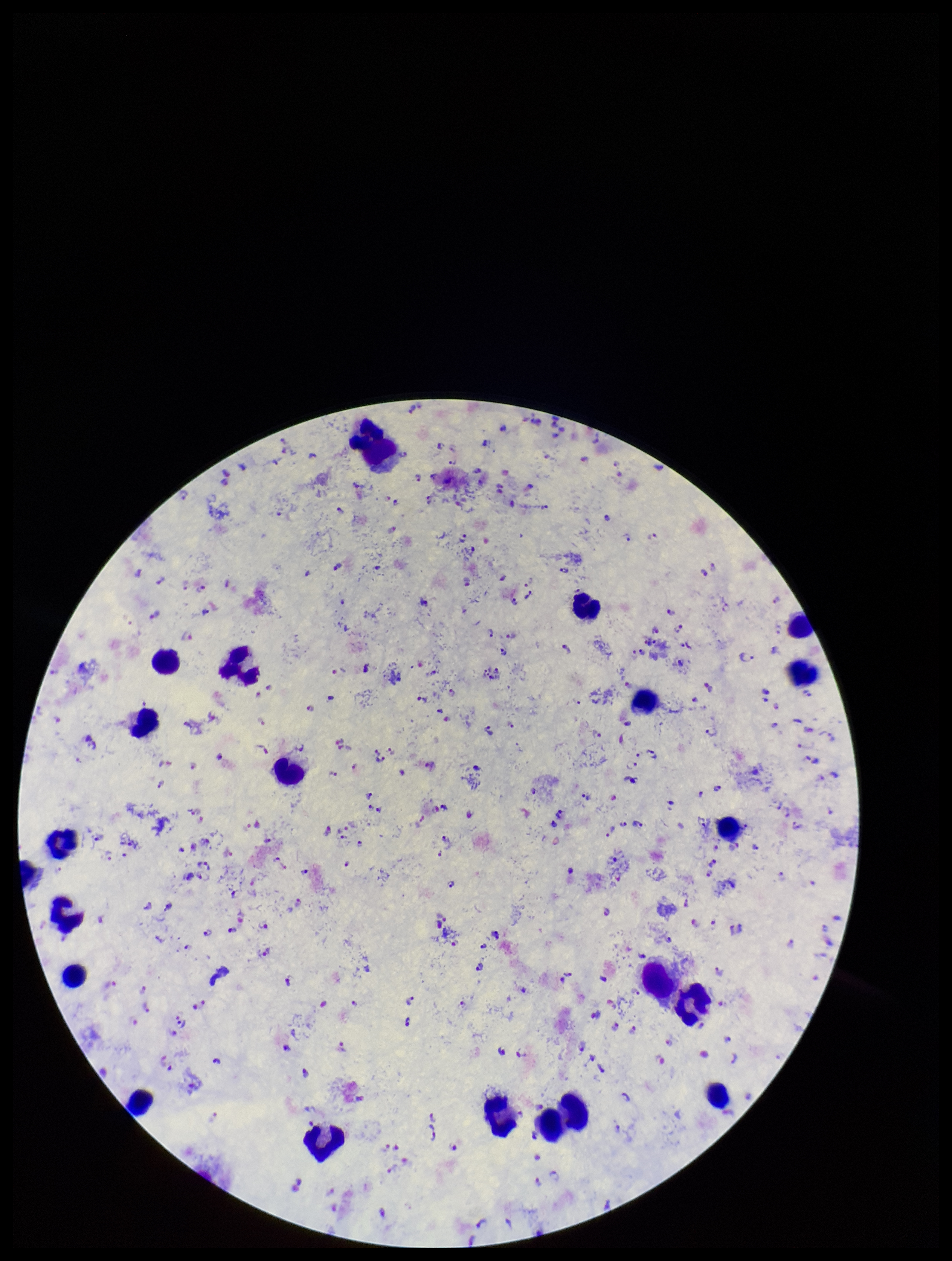 Leukocyte count: 19. Giemsa stain. Patient malaria status: infected. Image is 952×1261 pixels. One field from this slide. Plasmodium parasites: detected. Preparation: thick smear. Smartphone photograph taken through the eyepiece of a microscope. Species reported for this patient: Plasmodium falciparum. Parasite count: 218.